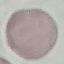
Malaria status: uninfected. Giemsa-stained preparation. Acquired by smartphone through the microscope eyepiece. Thin smear of blood. Automatically extracted cell patch, resized to 64 × 64 pixels.